Report the malaria status of this cell.
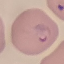
Parasitized.

stain = Giemsa
capture = smartphone through the microscope eyepiece
preparation = thin blood smear
image type = cell patch, automatically extracted from a larger field of view and resized to 64 × 64 pixels